Locate and identify every blood parasite.
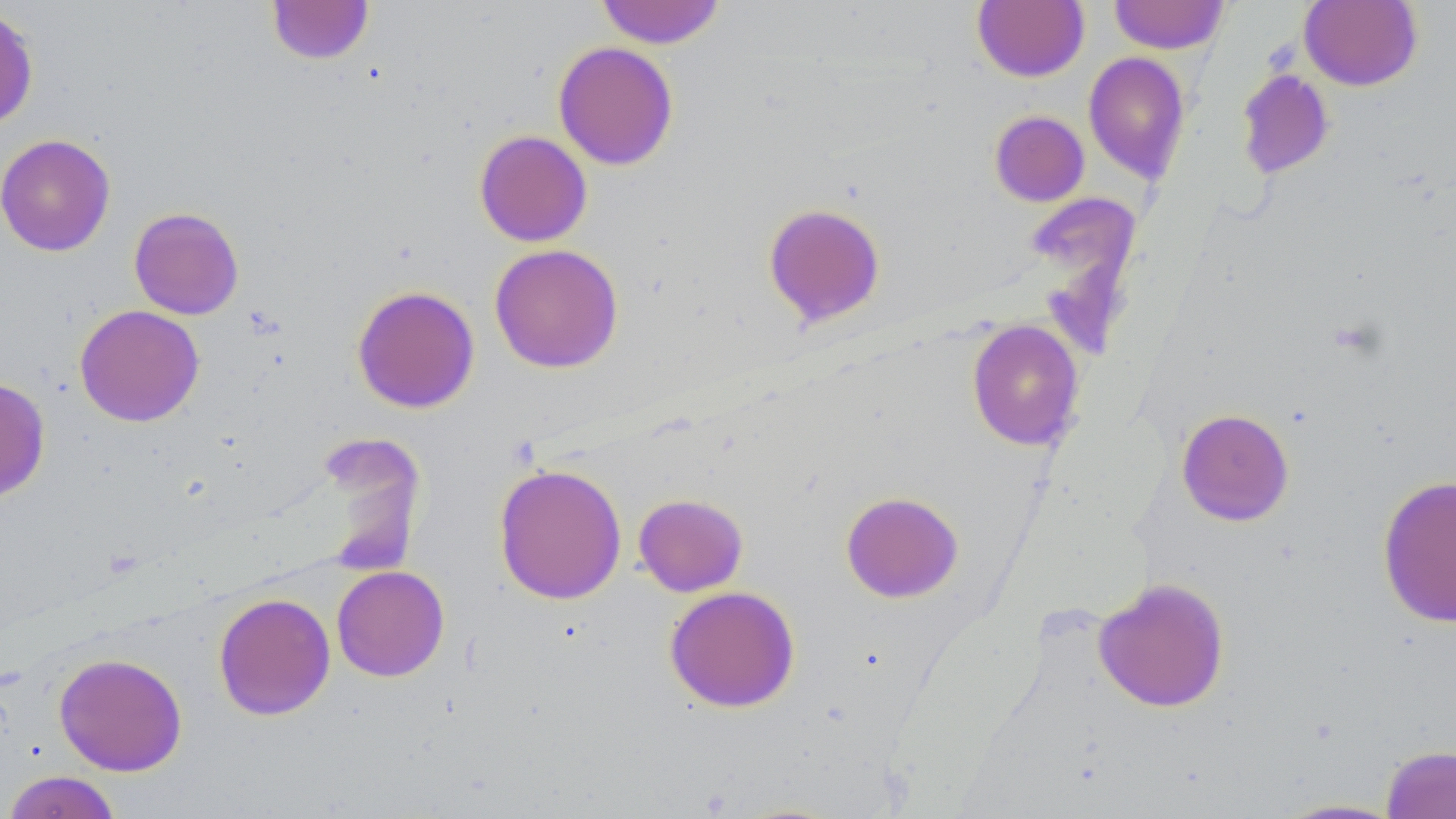
No blood parasites observed.

{
  "slide_level_diagnosis": "negative for blood parasites",
  "image_size": "1456×819 pixels",
  "uninfected_red_blood_cell_locations": "approximate bounding boxes as (x1, y1, x2, y2) in pixels: (595, 0, 726, 49), (1109, 0, 1230, 55), (266, 1, 375, 64), (972, 1, 1089, 82), (1299, 1, 1423, 91), (0, 5, 39, 130), (552, 41, 678, 170), (1083, 52, 1191, 183), (1236, 69, 1335, 180), (989, 110, 1090, 207), (474, 129, 592, 247), (0, 133, 116, 256), (1023, 193, 1142, 306), (762, 202, 887, 329), (129, 206, 244, 320), (488, 244, 624, 374), (351, 284, 480, 414), (74, 304, 204, 427), (966, 319, 1085, 451), (0, 376, 51, 503), (1176, 408, 1294, 526), (322, 431, 424, 576), (493, 462, 627, 604), (1376, 474, 1456, 629), (840, 491, 964, 603), (633, 493, 748, 597), (331, 565, 449, 681), (1093, 578, 1230, 712), (664, 585, 801, 713), (213, 592, 336, 720), (53, 652, 188, 776), (1381, 744, 1456, 819), (2, 770, 123, 819), (1270, 797, 1410, 818)",
  "preparation": "thin blood smear",
  "modality": "light microscopy",
  "magnification": "1000x",
  "field_of_view": "single",
  "stain": "May-Grünwald-Giemsa"
}